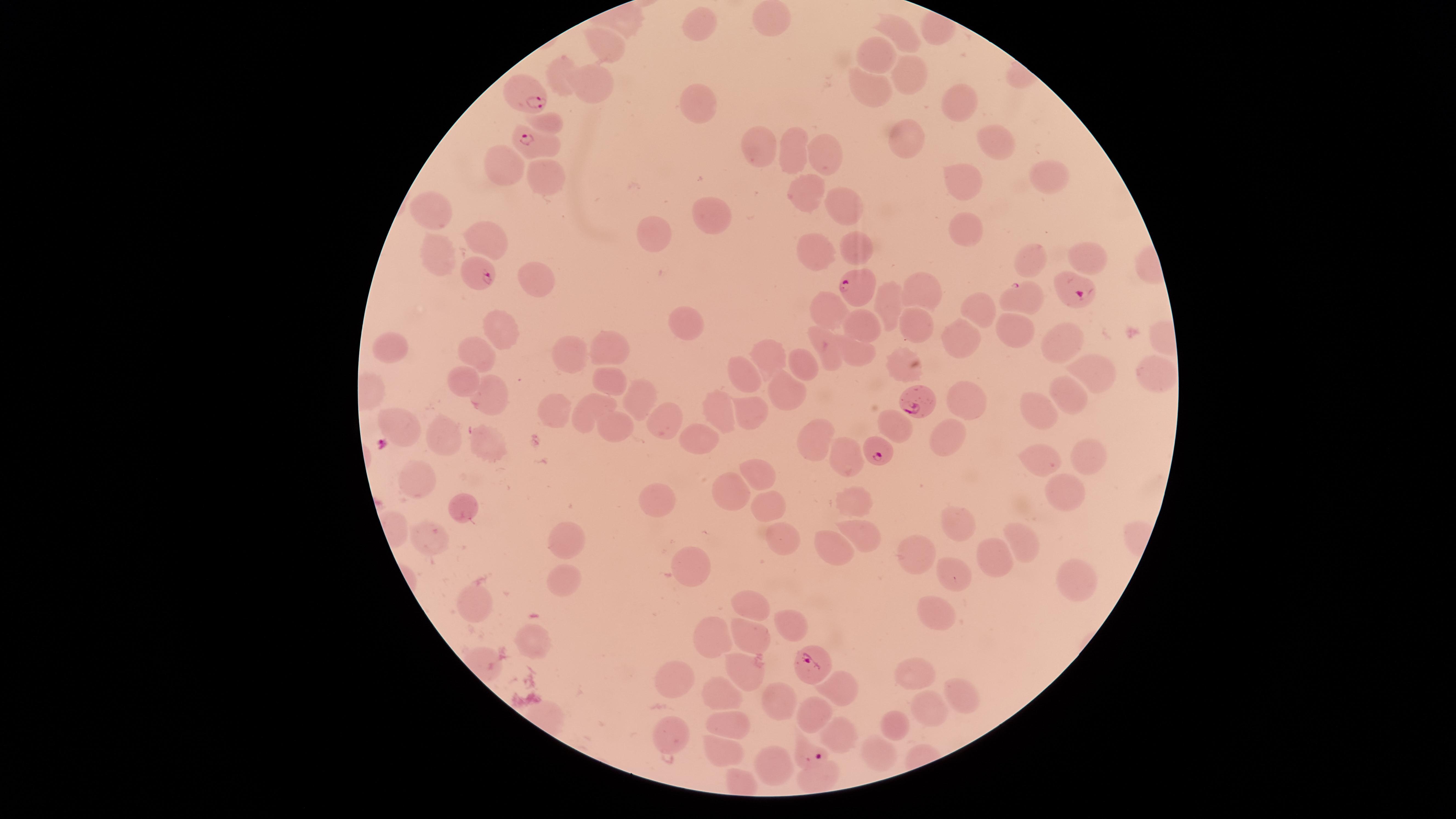

Approximate marker points as [x, y] in pixels.
Summary:
  - Parasitized RBCs: [523, 95], [523, 136], [478, 275], [1068, 288], [853, 290], [913, 404], [873, 451], [809, 662], [809, 753]
  - Uninfected RBCs: [768, 18], [701, 27], [903, 34], [607, 42], [867, 51], [564, 68], [906, 68], [597, 81], [867, 85], [692, 97], [957, 103], [547, 118], [903, 138], [757, 144], [991, 146], [798, 148], [824, 150], [499, 167], [1052, 172], [544, 178], [795, 178], [969, 183], [846, 208], [436, 212], [717, 213], [960, 231], [483, 235], [653, 235], [851, 245], [821, 247], [439, 256], [1091, 256], [1027, 258], [534, 280], [916, 286], [1023, 299], [892, 300], [975, 311], [832, 312], [911, 315], [1009, 322], [504, 324], [859, 325], [680, 328], [961, 336], [1051, 336], [611, 343], [395, 349], [766, 351], [829, 352], [571, 353], [479, 354], [898, 359], [859, 360], [798, 362], [745, 368], [1089, 369], [1153, 372], [461, 377], [607, 381], [1064, 384], [635, 388], [790, 393], [490, 395], [964, 396], [1035, 406], [597, 408], [717, 409], [752, 411], [564, 412], [661, 423], [404, 424], [616, 424], [702, 434], [943, 435], [442, 438], [813, 438], [490, 442], [1084, 448], [850, 455], [1041, 465], [750, 472], [418, 481], [1060, 483], [730, 495], [853, 497], [652, 499], [771, 506], [468, 509], [961, 519], [853, 531], [567, 539], [429, 540], [790, 541], [1015, 541], [836, 548], [920, 554], [994, 557], [682, 561], [952, 571], [1074, 572], [567, 580], [480, 597], [750, 605], [936, 609], [789, 624], [713, 635], [752, 638], [534, 641], [747, 664], [915, 673], [679, 674], [839, 687], [718, 694], [785, 698], [961, 700], [815, 705], [925, 708], [729, 721], [903, 727], [673, 729], [842, 735], [717, 748], [879, 751], [771, 765], [820, 775]
  - Field of view: single
  - Visible region: circular
  - Preparation: thin smear of blood
  - Capture: smartphone photograph through the microscope eyepiece
  - Image size: 1456×819 pixels
  - Stain: Giemsa
  - Presence: malaria parasites seen
  - Species: Plasmodium falciparum